Point out each malaria parasite and each leukocyte.
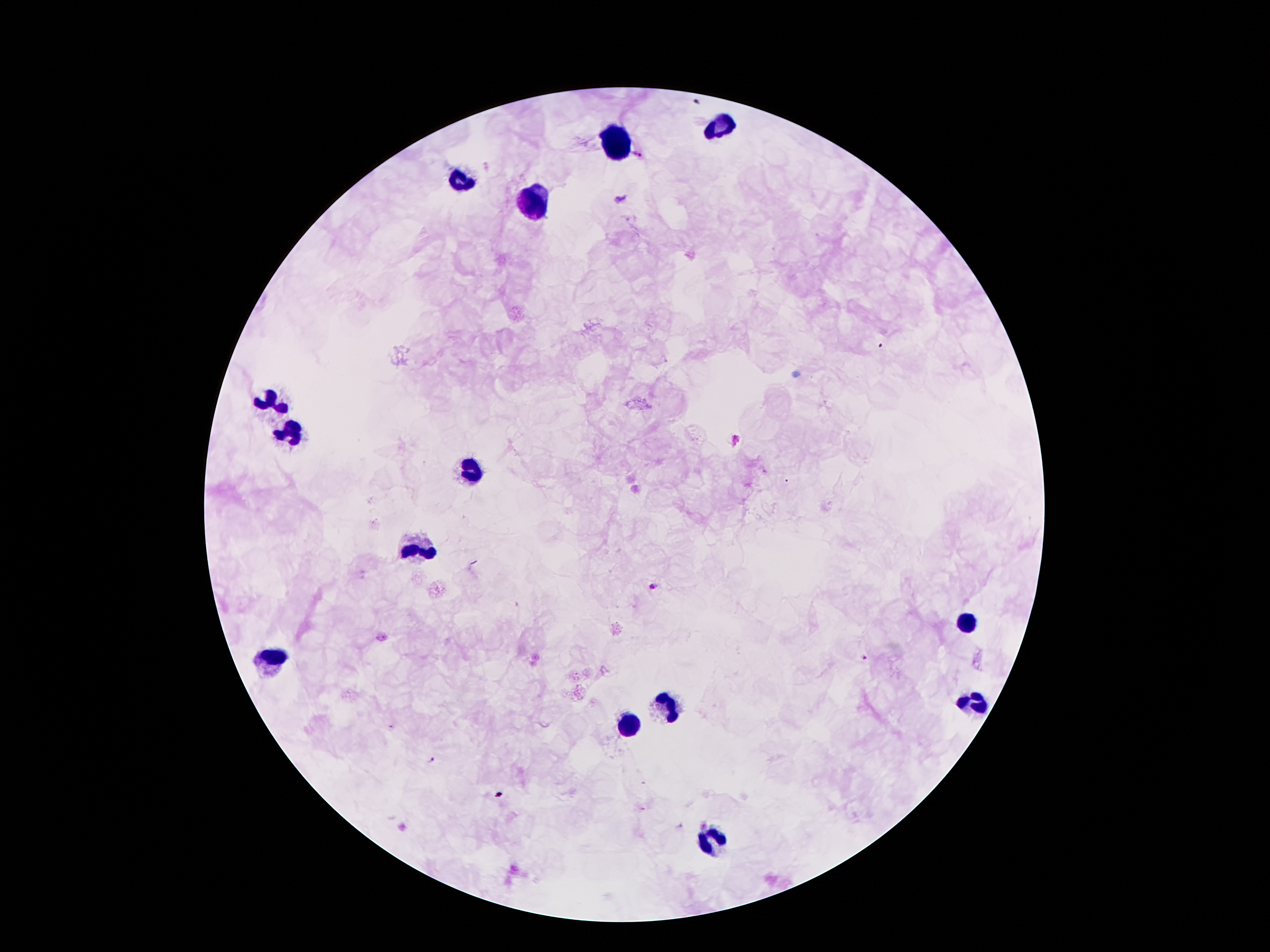
Approximate centers as [x, y] in pixels.
Malaria parasites: [639, 154], [652, 587], [863, 656], [431, 761].
Leukocytes: [723, 123], [618, 144], [464, 180], [536, 205], [269, 402], [290, 432], [471, 468], [413, 550], [965, 621], [272, 655], [975, 701], [667, 703], [627, 724], [709, 841].

100x magnification. One field from this slide. Giemsa stain. Patient malaria status: positive for Plasmodium falciparum. Image is 1270×952 pixels. Thick blood smear. Photographed through the microscope eyepiece with a smartphone camera.